Name the blood parasite species.
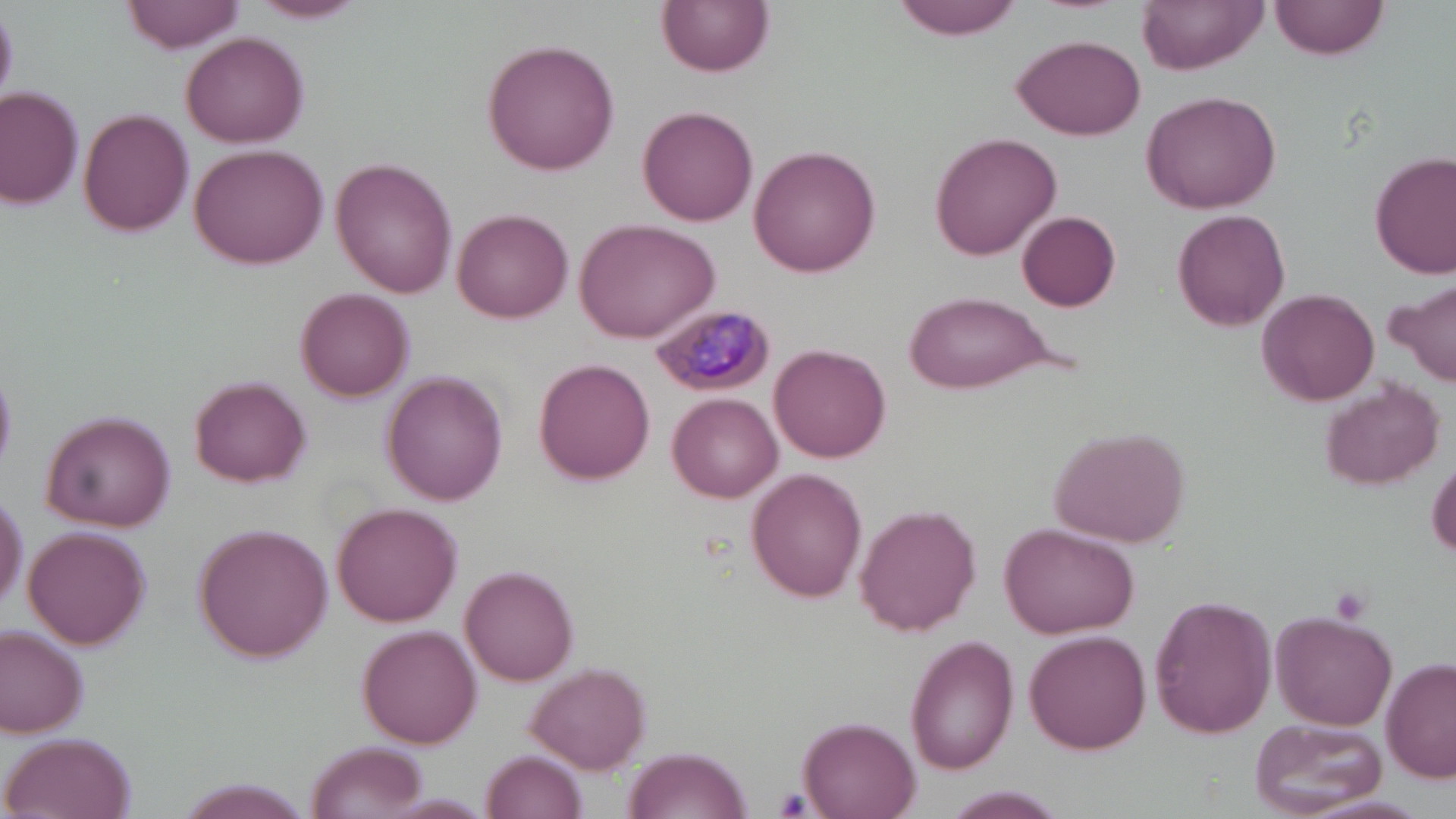
Plasmodium malariae.

Approximate bounding boxes as named x1/y1/x2/y2 corners in pixels. Plasmodium malariae-infected red blood cell locations: (x1=649, y1=301, x2=776, y2=398). Platelet locations: (x1=1329, y1=584, x2=1373, y2=626), (x1=774, y1=789, x2=815, y2=816). Uninfected red blood cell locations: (x1=124, y1=0, x2=246, y2=54), (x1=251, y1=0, x2=368, y2=22), (x1=659, y1=0, x2=773, y2=76), (x1=894, y1=0, x2=1024, y2=41), (x1=1139, y1=0, x2=1268, y2=73), (x1=1271, y1=0, x2=1388, y2=59), (x1=181, y1=31, x2=309, y2=148), (x1=1013, y1=34, x2=1145, y2=140), (x1=483, y1=38, x2=622, y2=176), (x1=1, y1=88, x2=83, y2=210), (x1=1140, y1=88, x2=1282, y2=215), (x1=637, y1=105, x2=758, y2=225), (x1=79, y1=109, x2=194, y2=236), (x1=929, y1=130, x2=1062, y2=260), (x1=190, y1=142, x2=329, y2=269), (x1=749, y1=145, x2=880, y2=278), (x1=1370, y1=150, x2=1456, y2=280), (x1=332, y1=159, x2=457, y2=298), (x1=452, y1=207, x2=573, y2=323), (x1=1173, y1=208, x2=1291, y2=332), (x1=1016, y1=210, x2=1121, y2=309), (x1=573, y1=217, x2=719, y2=343), (x1=1391, y1=280, x2=1455, y2=386), (x1=1257, y1=287, x2=1380, y2=406), (x1=296, y1=288, x2=413, y2=400), (x1=900, y1=291, x2=1062, y2=394), (x1=772, y1=344, x2=890, y2=461), (x1=534, y1=359, x2=653, y2=481), (x1=382, y1=371, x2=508, y2=504), (x1=190, y1=376, x2=311, y2=487), (x1=1320, y1=380, x2=1445, y2=492), (x1=669, y1=393, x2=781, y2=502), (x1=39, y1=411, x2=177, y2=531), (x1=1049, y1=424, x2=1192, y2=547), (x1=1428, y1=456, x2=1456, y2=562), (x1=746, y1=469, x2=868, y2=601), (x1=0, y1=493, x2=26, y2=614), (x1=333, y1=503, x2=461, y2=626), (x1=857, y1=504, x2=981, y2=635), (x1=1002, y1=522, x2=1138, y2=639), (x1=24, y1=526, x2=150, y2=650), (x1=196, y1=526, x2=334, y2=661), (x1=460, y1=565, x2=579, y2=685), (x1=1149, y1=594, x2=1277, y2=738), (x1=1272, y1=611, x2=1398, y2=730), (x1=0, y1=625, x2=89, y2=738), (x1=360, y1=625, x2=482, y2=749), (x1=1024, y1=630, x2=1151, y2=754), (x1=906, y1=634, x2=1015, y2=773), (x1=1381, y1=658, x2=1456, y2=783), (x1=525, y1=661, x2=652, y2=773), (x1=799, y1=716, x2=922, y2=817), (x1=1251, y1=718, x2=1387, y2=816), (x1=2, y1=734, x2=132, y2=819), (x1=305, y1=741, x2=428, y2=818), (x1=623, y1=746, x2=752, y2=819), (x1=481, y1=750, x2=586, y2=819), (x1=177, y1=779, x2=307, y2=818), (x1=944, y1=787, x2=1068, y2=816), (x1=379, y1=795, x2=495, y2=817). Image is 1456×819 pixels. Captured at 1000x magnification. Thin blood smear. May-Grünwald-Giemsa stain. One field of a larger specimen. Light microscopy.